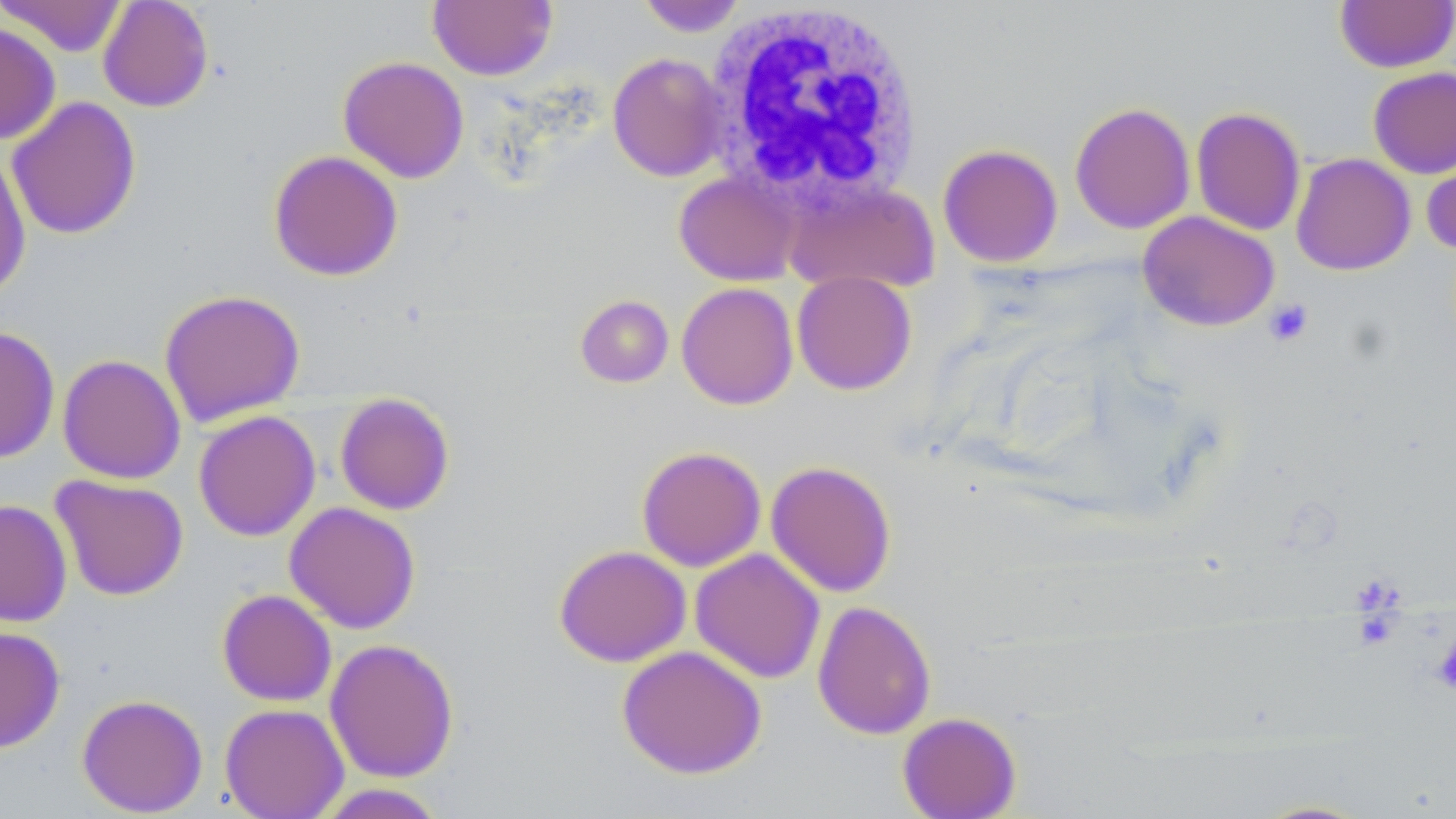
slide-level diagnosis = no evidence of blood parasites
platelet locations = approximate bounding boxes as [x1, y1, x2, y2] in pixels: [1264, 299, 1314, 347], [1433, 634, 1456, 694]
modality = light microscopy
white blood cell locations = approximate bounding boxes as [x1, y1, x2, y2] in pixels: [701, 2, 921, 208]
magnification = 1000x
image size = 1456×819 pixels
uninfected red blood cell locations = approximate bounding boxes as [x1, y1, x2, y2] in pixels: [1, 0, 128, 56], [97, 0, 214, 112], [427, 0, 558, 81], [636, 0, 748, 36], [1335, 0, 1456, 73], [0, 20, 60, 145], [607, 52, 729, 182], [338, 56, 469, 183], [1368, 66, 1456, 179], [6, 95, 141, 241], [1069, 101, 1196, 234], [1190, 106, 1306, 236], [1421, 140, 1456, 257], [937, 144, 1063, 268], [0, 147, 30, 299], [268, 150, 403, 282], [1291, 153, 1416, 275], [674, 170, 801, 286], [784, 180, 940, 294], [1137, 210, 1280, 332], [791, 270, 917, 395], [676, 282, 799, 410], [159, 288, 305, 427], [575, 294, 674, 388], [0, 325, 60, 463], [57, 354, 186, 484], [334, 392, 455, 515], [192, 405, 454, 525], [193, 410, 321, 541], [636, 446, 767, 571], [765, 460, 897, 597], [49, 474, 189, 601], [0, 499, 73, 627], [284, 502, 421, 634], [554, 544, 691, 667], [689, 548, 826, 684], [216, 588, 337, 707], [812, 600, 936, 740], [0, 625, 66, 753], [324, 638, 459, 783], [617, 645, 767, 778], [76, 694, 208, 816], [220, 703, 349, 818], [896, 712, 1021, 818], [311, 784, 450, 818], [1247, 799, 1381, 818]
stain = May-Grünwald-Giemsa
preparation = thin blood film
field of view = one of a larger specimen